Assess the morphology of the erythrocytes.
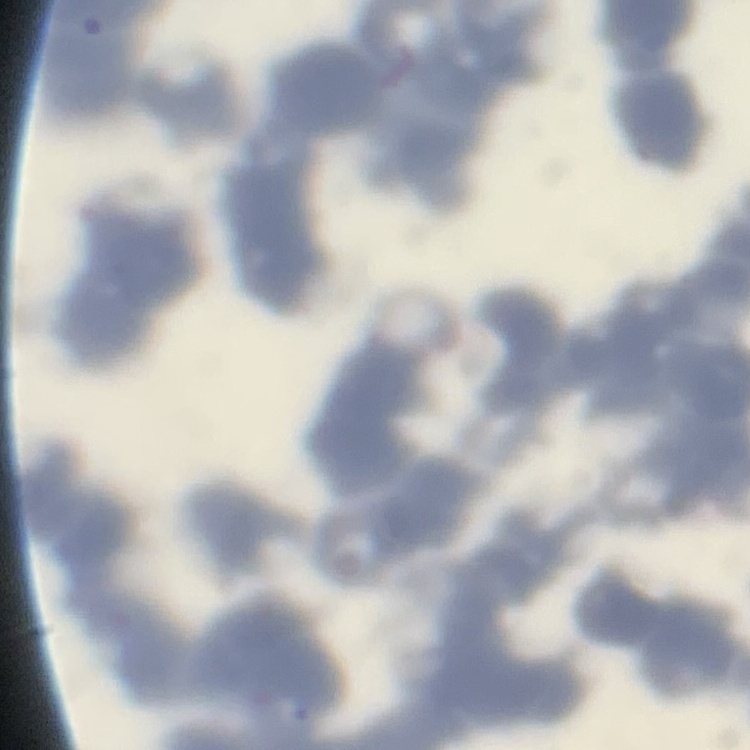

Rouleaux formation.

stain = Field's or Giemsa
image type = one tile cut from a larger photomicrograph
preparation = thin blood smear